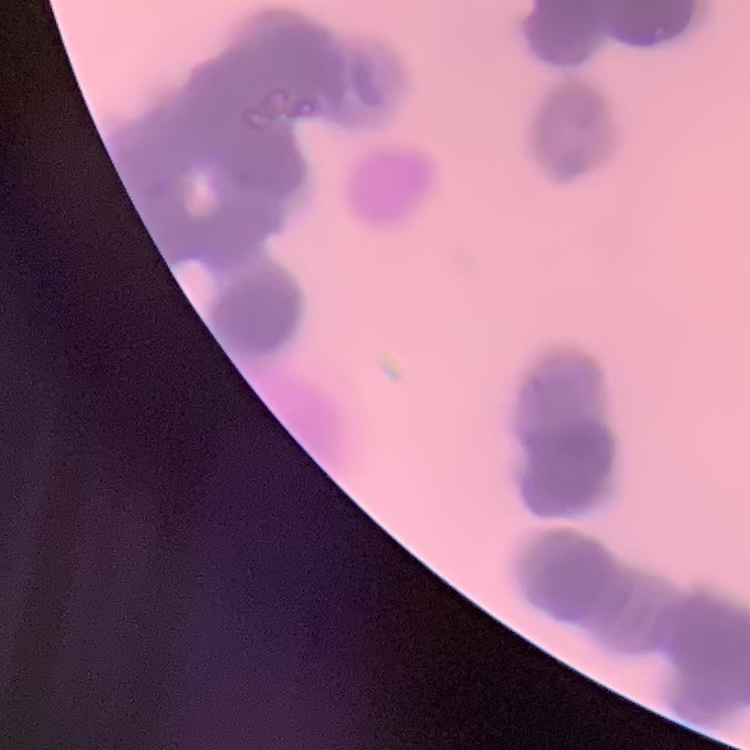
The red blood cells exhibit rouleaux formation. Stained with either Field's or Giemsa. One tile cut from a larger photomicrograph. Thin blood film.